Identify the preparation type.
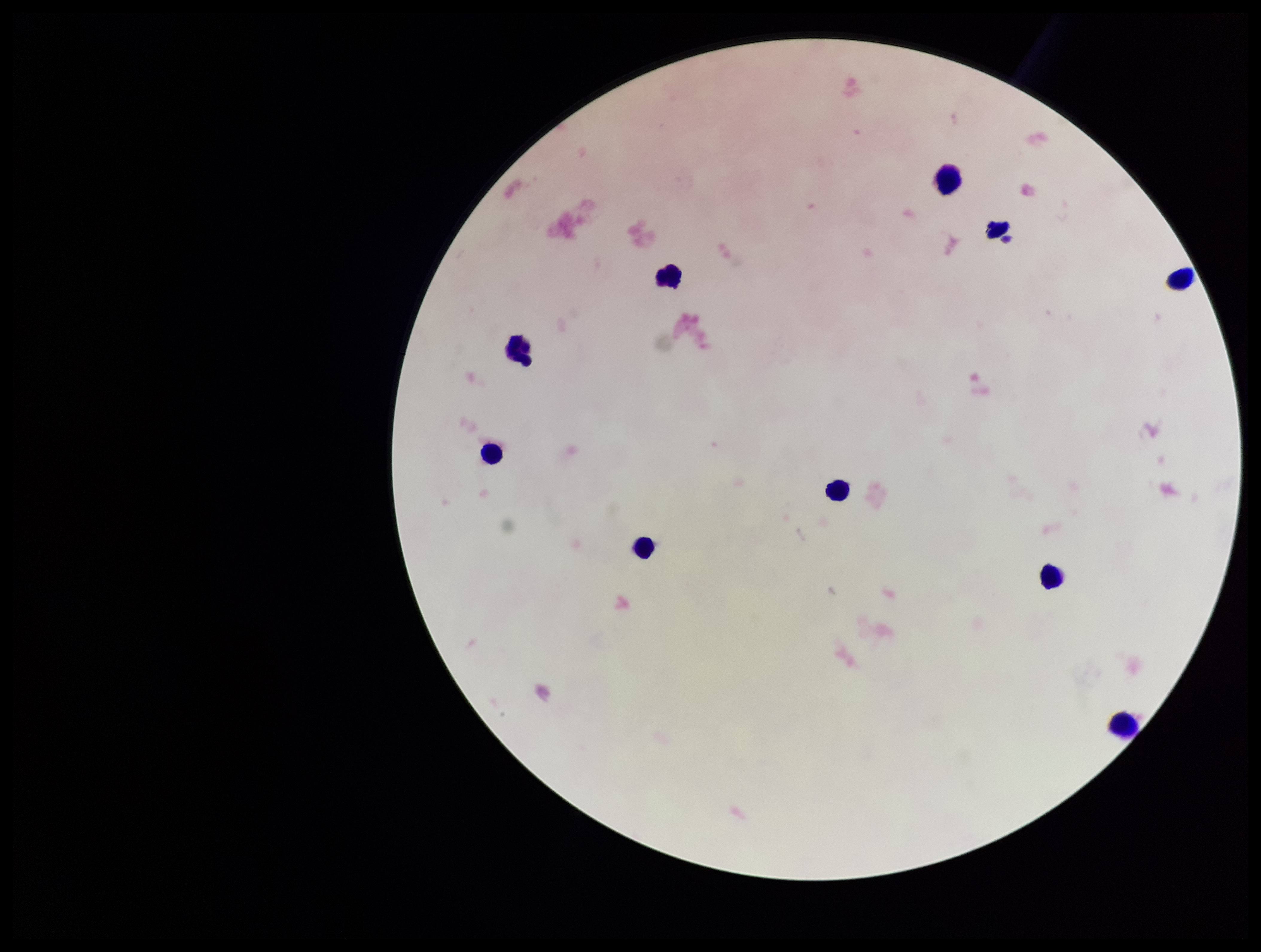

A thick smear.

Leukocyte count: 9. One field from this slide. Patient malaria status: negative. Photographed through the microscope eyepiece with a smartphone camera. Parasite count: 0. Plasmodium parasites: none seen. Giemsa stain. Image is 1261×952 pixels.